State which cell type is depicted.
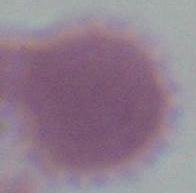

An erythrocyte.

{
  "modality": "micrograph",
  "magnification": "1000x"
}